Find each parasitized red blood cell.
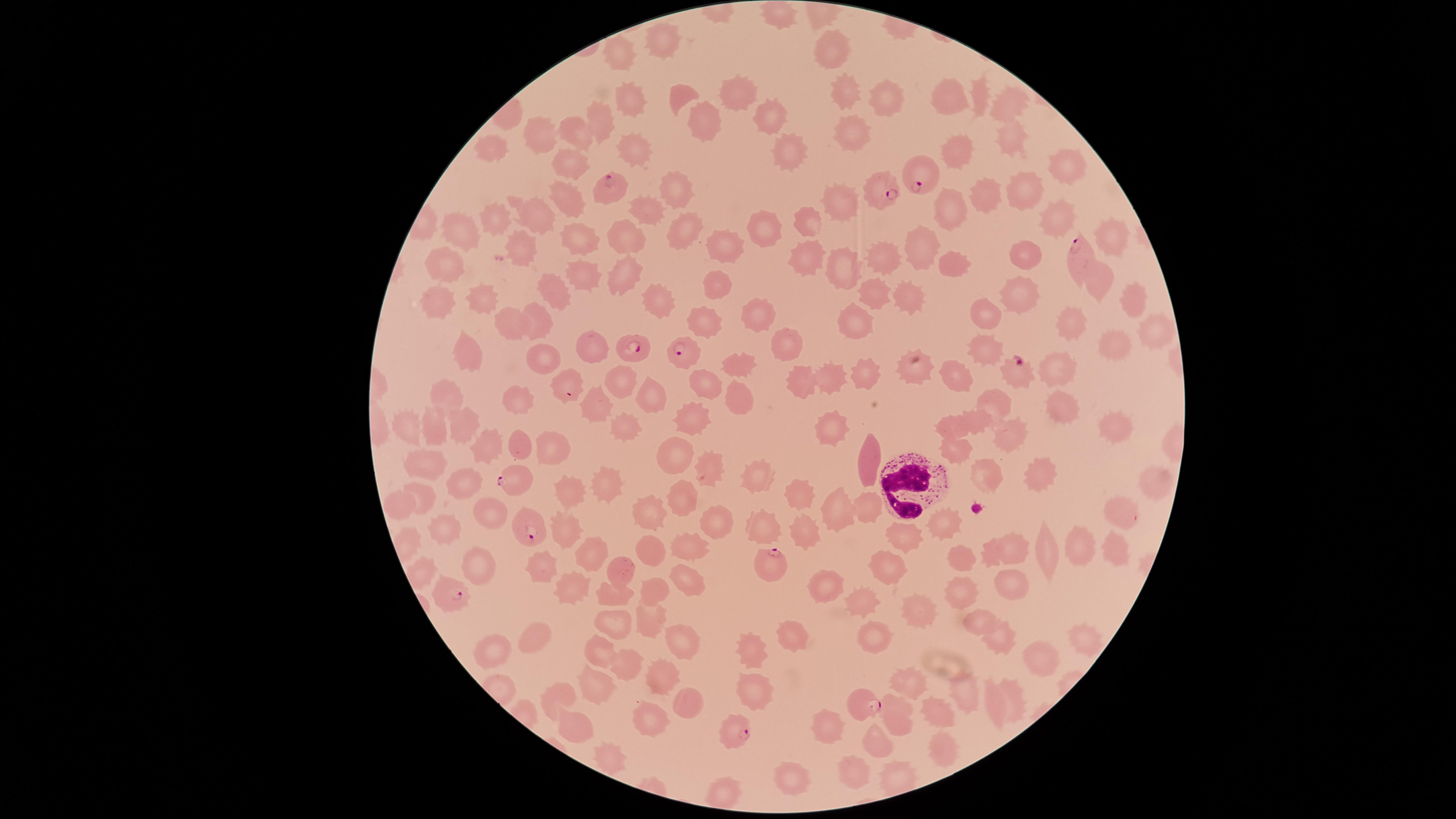
Approximate marker points, in pixels from the top-left corner.
Parasitized red blood cells: (x=926, y=182), (x=610, y=186), (x=880, y=189), (x=1072, y=253), (x=639, y=349), (x=685, y=350), (x=1019, y=373), (x=511, y=482), (x=527, y=529), (x=767, y=565), (x=451, y=597), (x=868, y=704), (x=731, y=731).

Approximate marker points, in pixels from the top-left corner.
Summary:
  - White blood cells: (x=901, y=482)
  - Uninfected red blood cells: (x=780, y=14), (x=835, y=50), (x=666, y=52), (x=622, y=54), (x=837, y=91), (x=741, y=93), (x=686, y=95), (x=882, y=98), (x=981, y=98), (x=947, y=99), (x=630, y=102), (x=1009, y=106), (x=767, y=118), (x=596, y=121), (x=705, y=121), (x=577, y=132), (x=544, y=135), (x=849, y=140), (x=1006, y=141), (x=954, y=143), (x=493, y=146), (x=636, y=147), (x=788, y=148), (x=563, y=159), (x=1061, y=166), (x=1024, y=189), (x=671, y=192), (x=568, y=193), (x=985, y=199), (x=846, y=206), (x=954, y=209), (x=539, y=212), (x=648, y=213), (x=497, y=216), (x=807, y=218), (x=1055, y=218), (x=774, y=227), (x=683, y=230), (x=627, y=232), (x=462, y=233), (x=576, y=235), (x=1108, y=237), (x=727, y=245), (x=524, y=246), (x=921, y=247), (x=1032, y=251), (x=807, y=252), (x=881, y=254), (x=956, y=261), (x=845, y=263), (x=447, y=265), (x=576, y=273), (x=630, y=273), (x=716, y=282), (x=1102, y=282), (x=872, y=291), (x=558, y=292), (x=1025, y=296), (x=666, y=297), (x=1137, y=297), (x=488, y=299), (x=908, y=301), (x=439, y=306), (x=539, y=314), (x=761, y=317), (x=990, y=317), (x=701, y=318), (x=511, y=322), (x=857, y=324), (x=1070, y=324), (x=1151, y=325), (x=788, y=341), (x=588, y=343), (x=1115, y=343), (x=463, y=353), (x=985, y=355), (x=547, y=356), (x=736, y=360), (x=864, y=366), (x=1059, y=367), (x=922, y=369), (x=839, y=371), (x=624, y=375), (x=707, y=378), (x=798, y=378), (x=569, y=379), (x=958, y=380), (x=449, y=391), (x=739, y=391), (x=651, y=392), (x=523, y=401), (x=1066, y=404), (x=592, y=406), (x=997, y=408), (x=690, y=417), (x=1114, y=418), (x=832, y=421), (x=976, y=421), (x=412, y=425), (x=622, y=427), (x=950, y=427), (x=1013, y=427), (x=435, y=430), (x=465, y=430), (x=546, y=446), (x=490, y=447), (x=518, y=447), (x=952, y=450), (x=676, y=458), (x=869, y=458), (x=429, y=461), (x=708, y=467), (x=1039, y=471), (x=983, y=474), (x=607, y=482), (x=756, y=485), (x=463, y=486), (x=1150, y=486), (x=565, y=491), (x=425, y=495), (x=677, y=498), (x=803, y=501), (x=394, y=503), (x=866, y=503), (x=1116, y=512), (x=488, y=515), (x=650, y=515), (x=833, y=515), (x=708, y=520), (x=443, y=521), (x=947, y=521), (x=766, y=528), (x=562, y=531), (x=800, y=532), (x=900, y=537), (x=692, y=544), (x=1078, y=546), (x=1014, y=549), (x=654, y=551), (x=589, y=553), (x=1047, y=553), (x=1111, y=555), (x=961, y=558), (x=469, y=568), (x=624, y=571), (x=885, y=571), (x=538, y=574), (x=686, y=581), (x=566, y=585), (x=1009, y=585), (x=654, y=589), (x=969, y=590), (x=613, y=593), (x=820, y=593), (x=857, y=600), (x=917, y=615), (x=612, y=618), (x=975, y=618), (x=647, y=619), (x=793, y=632), (x=1082, y=633), (x=880, y=635), (x=533, y=636), (x=677, y=639), (x=993, y=639), (x=753, y=647), (x=494, y=654), (x=1039, y=655), (x=604, y=658), (x=624, y=670), (x=664, y=681), (x=595, y=686), (x=911, y=686), (x=753, y=691), (x=965, y=693), (x=559, y=694), (x=1012, y=695), (x=992, y=706), (x=686, y=707), (x=940, y=709), (x=900, y=716), (x=650, y=720), (x=570, y=725), (x=823, y=728), (x=876, y=738), (x=938, y=744), (x=602, y=757), (x=857, y=769), (x=792, y=775), (x=726, y=792)
  - Image size: 1456×819 pixels
  - Stain: Giemsa
  - Capture: smartphone photograph through the microscope eyepiece
  - Visible region: circular
  - Species: Plasmodium falciparum
  - Preparation: thin blood smear
  - Field of view: single